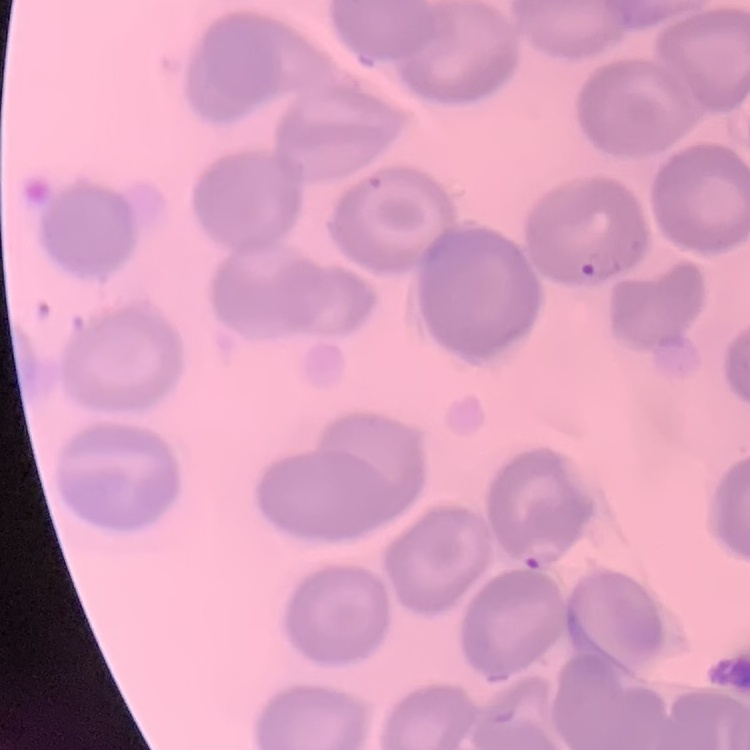
red blood cell morphology = no rouleaux formation
image type = one tile cut from a larger photomicrograph
preparation = thin blood film
stain = Field's or Giemsa